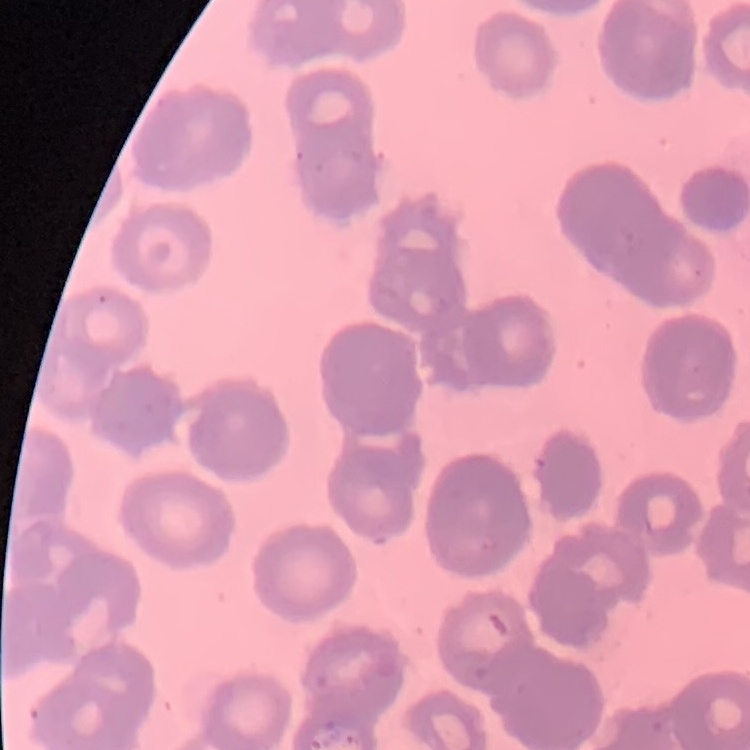

The erythrocytes show rouleaux formation. Stained with either Field's or Giemsa. Thin blood smear. One tile cut from a larger photomicrograph.